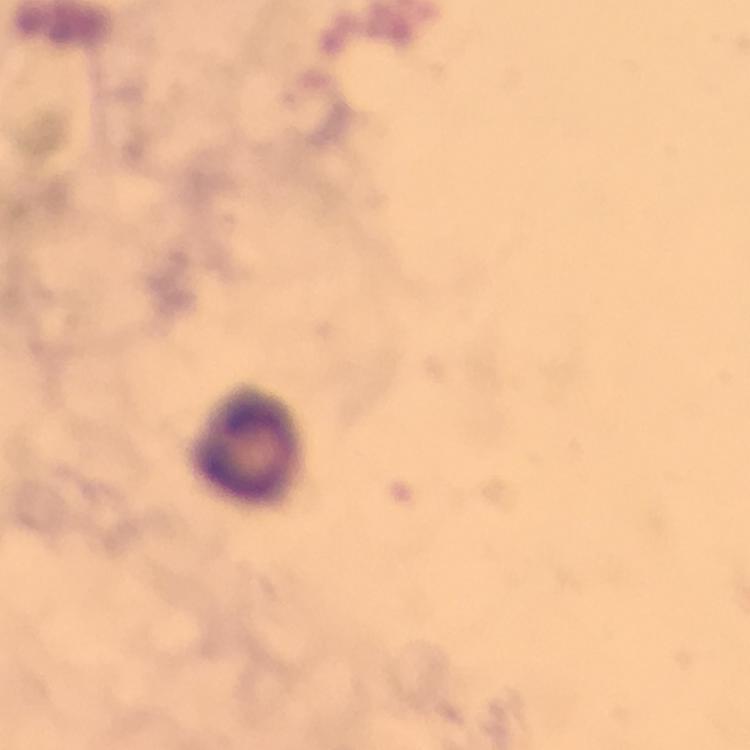

leukocyte locations = approximate centers as [x, y] in pixels: [247, 449]
immersion oil = used
capture = smartphone mounted on the microscope
stain = Giemsa
magnification = 100x
preparation = thick smear
context = from a malaria diagnostic workup
cropped from = one field of view
image size = 750×750 pixels
Plasmodium parasites = none seen